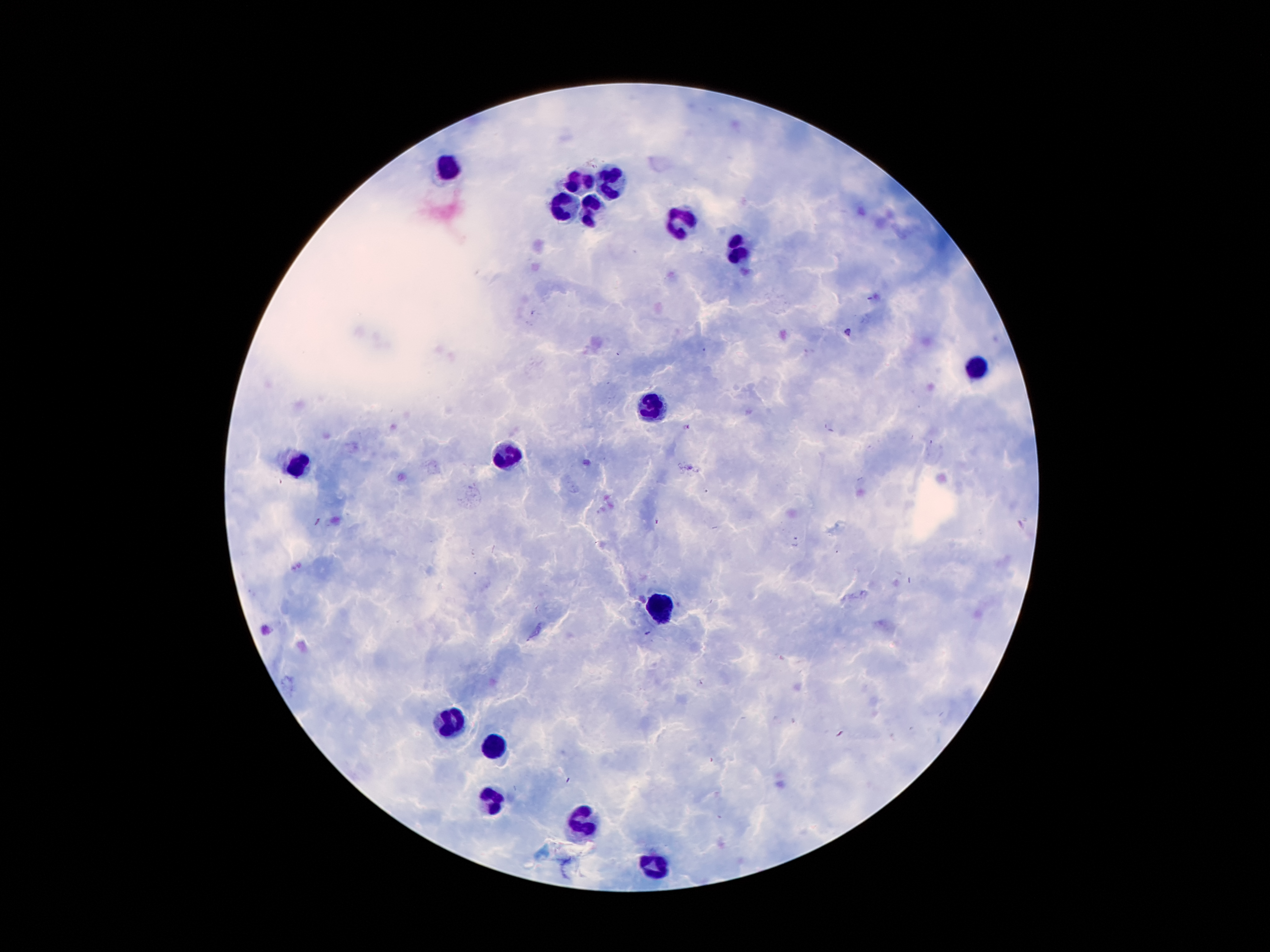
Approximate centers as (x, y) in pixels. Plasmodium parasite locations: (869, 298), (847, 331), (656, 520), (317, 522), (648, 633). Leukocyte locations: (454, 162), (575, 177), (615, 177), (561, 204), (592, 208), (678, 223), (741, 255), (974, 370), (651, 404), (508, 458), (300, 465), (664, 607), (452, 723), (496, 746), (491, 800), (580, 826), (655, 868). 100x magnification. Smartphone photograph taken through the microscope eyepiece. Thick blood smear. Image is 1270×952 pixels. Single field of view. Patient malaria status: infected with Plasmodium falciparum. Giemsa-stained preparation.